Identify the cell.
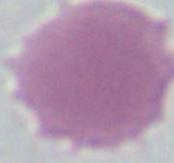
This is an erythrocyte.

magnification = 1000x
modality = micrograph